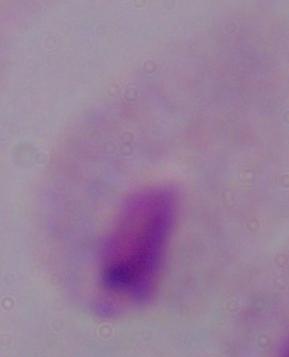

Photomicrograph. 1000x magnification. A trichomonad is seen.